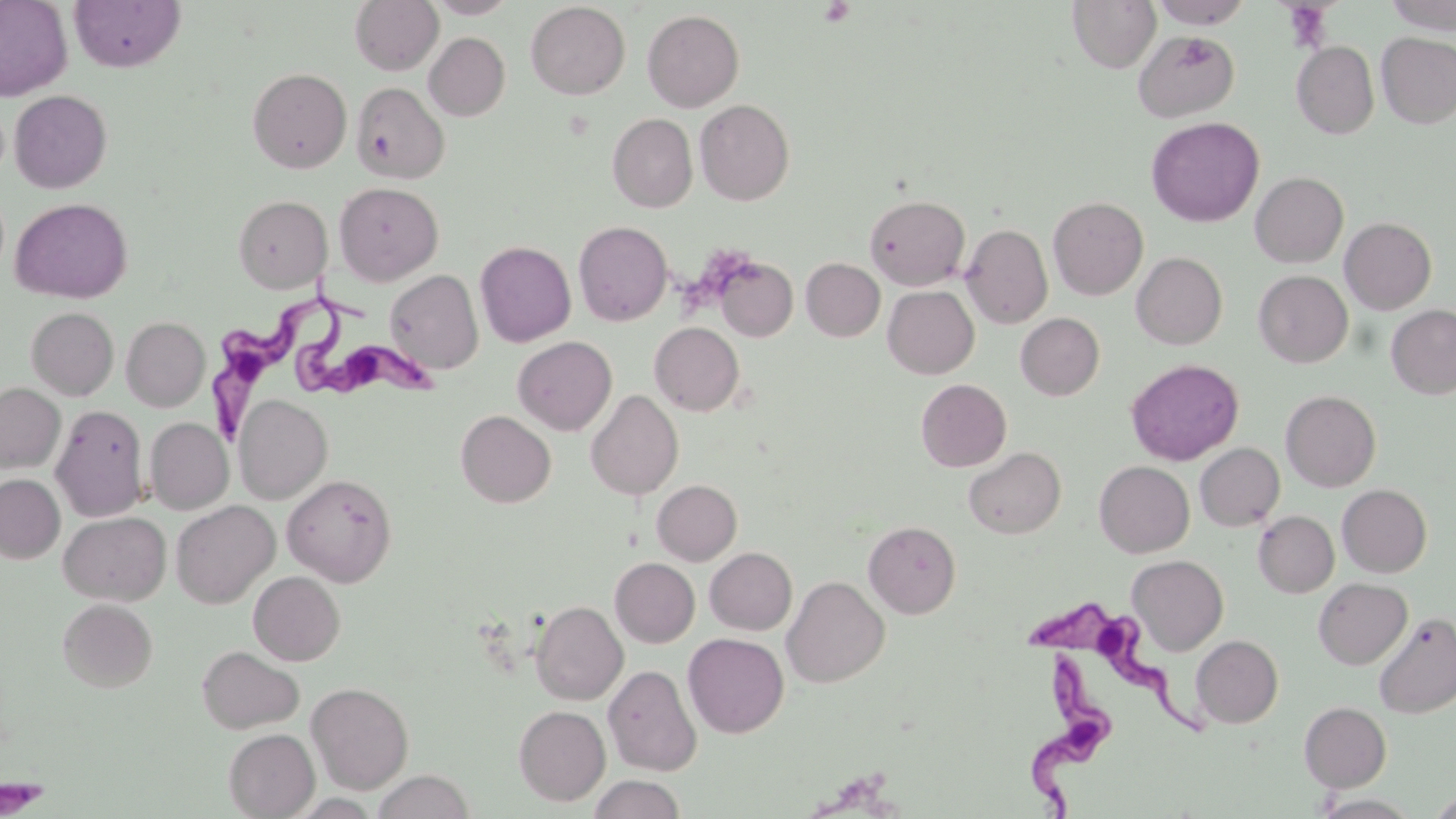
Summary:
  - Coordinate format: approximate bounding boxes as named x1/y1/x2/y2 corners in pixels
  - Platelet locations: (x1=819, y1=1, x2=854, y2=27), (x1=0, y1=777, x2=46, y2=817)
  - Trypanosoma brucei locations: (x1=303, y1=271, x2=449, y2=403), (x1=205, y1=290, x2=367, y2=440), (x1=1027, y1=596, x2=1204, y2=738), (x1=1023, y1=651, x2=1115, y2=819)
  - Uninfected red blood cell locations: (x1=0, y1=0, x2=73, y2=101), (x1=69, y1=0, x2=186, y2=72), (x1=350, y1=0, x2=443, y2=75), (x1=427, y1=0, x2=516, y2=18), (x1=1067, y1=0, x2=1161, y2=73), (x1=1151, y1=0, x2=1253, y2=29), (x1=1383, y1=0, x2=1455, y2=34), (x1=526, y1=2, x2=630, y2=99), (x1=642, y1=9, x2=745, y2=112), (x1=1134, y1=28, x2=1240, y2=122), (x1=424, y1=32, x2=510, y2=120), (x1=1376, y1=32, x2=1456, y2=128), (x1=1291, y1=41, x2=1379, y2=139), (x1=247, y1=68, x2=351, y2=173), (x1=351, y1=82, x2=449, y2=184), (x1=9, y1=89, x2=112, y2=193), (x1=695, y1=99, x2=794, y2=205), (x1=608, y1=113, x2=697, y2=212), (x1=1146, y1=116, x2=1264, y2=227), (x1=1250, y1=172, x2=1348, y2=267), (x1=334, y1=182, x2=443, y2=284), (x1=864, y1=193, x2=969, y2=290), (x1=233, y1=195, x2=332, y2=293), (x1=10, y1=197, x2=132, y2=303), (x1=1048, y1=197, x2=1148, y2=300), (x1=1340, y1=217, x2=1436, y2=314), (x1=574, y1=221, x2=673, y2=326), (x1=962, y1=223, x2=1053, y2=328), (x1=475, y1=241, x2=576, y2=347), (x1=1132, y1=252, x2=1228, y2=350), (x1=715, y1=255, x2=799, y2=342), (x1=801, y1=258, x2=885, y2=341), (x1=385, y1=269, x2=483, y2=374), (x1=1253, y1=270, x2=1353, y2=367), (x1=883, y1=285, x2=979, y2=378), (x1=1386, y1=305, x2=1456, y2=399), (x1=26, y1=307, x2=119, y2=399), (x1=1016, y1=313, x2=1104, y2=400), (x1=121, y1=317, x2=210, y2=411), (x1=650, y1=322, x2=744, y2=415), (x1=512, y1=336, x2=617, y2=435), (x1=1126, y1=358, x2=1244, y2=465), (x1=916, y1=379, x2=1011, y2=471), (x1=0, y1=383, x2=65, y2=473), (x1=586, y1=389, x2=683, y2=500), (x1=1281, y1=390, x2=1381, y2=492), (x1=234, y1=395, x2=332, y2=504), (x1=51, y1=404, x2=149, y2=520), (x1=456, y1=410, x2=556, y2=507), (x1=146, y1=417, x2=233, y2=514), (x1=1195, y1=443, x2=1285, y2=530), (x1=963, y1=447, x2=1066, y2=539), (x1=1094, y1=461, x2=1194, y2=557), (x1=0, y1=474, x2=65, y2=563), (x1=283, y1=474, x2=397, y2=586), (x1=652, y1=480, x2=742, y2=564), (x1=1337, y1=484, x2=1432, y2=577), (x1=171, y1=500, x2=279, y2=608), (x1=58, y1=511, x2=171, y2=604), (x1=1254, y1=511, x2=1339, y2=597), (x1=864, y1=520, x2=961, y2=618), (x1=705, y1=547, x2=797, y2=635), (x1=1127, y1=554, x2=1228, y2=655), (x1=610, y1=558, x2=700, y2=647), (x1=248, y1=571, x2=346, y2=665), (x1=783, y1=576, x2=890, y2=687), (x1=1314, y1=578, x2=1412, y2=669), (x1=57, y1=598, x2=158, y2=692), (x1=531, y1=600, x2=628, y2=705), (x1=1373, y1=612, x2=1456, y2=718), (x1=683, y1=633, x2=789, y2=738), (x1=1191, y1=635, x2=1283, y2=728), (x1=197, y1=645, x2=304, y2=734), (x1=603, y1=664, x2=702, y2=776), (x1=306, y1=681, x2=414, y2=794), (x1=1299, y1=701, x2=1391, y2=791), (x1=514, y1=705, x2=610, y2=806), (x1=224, y1=728, x2=319, y2=818), (x1=372, y1=770, x2=475, y2=818), (x1=587, y1=775, x2=686, y2=819), (x1=1429, y1=793, x2=1456, y2=817), (x1=1311, y1=794, x2=1421, y2=819)
  - Slide-level diagnosis: Trypanosoma brucei
  - Field of view: one of a larger specimen
  - Image size: 1456×819 pixels
  - Preparation: thin blood smear
  - Modality: optical microscopy
  - Magnification: 1000x
  - Stain: May-Grünwald-Giemsa